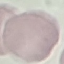
Result: no malaria parasites detected. Thin blood film. Acquired by smartphone through the microscope eyepiece. Giemsa stain. Cell patch, automatically extracted from a larger field of view and resized to 64 × 64 pixels.